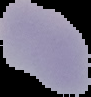
image size = 91×97 pixels
image type = segmented cell region with the area outside set to black
result = no malaria parasites seen
preparation = thin blood film